Identify the blood parasite species.
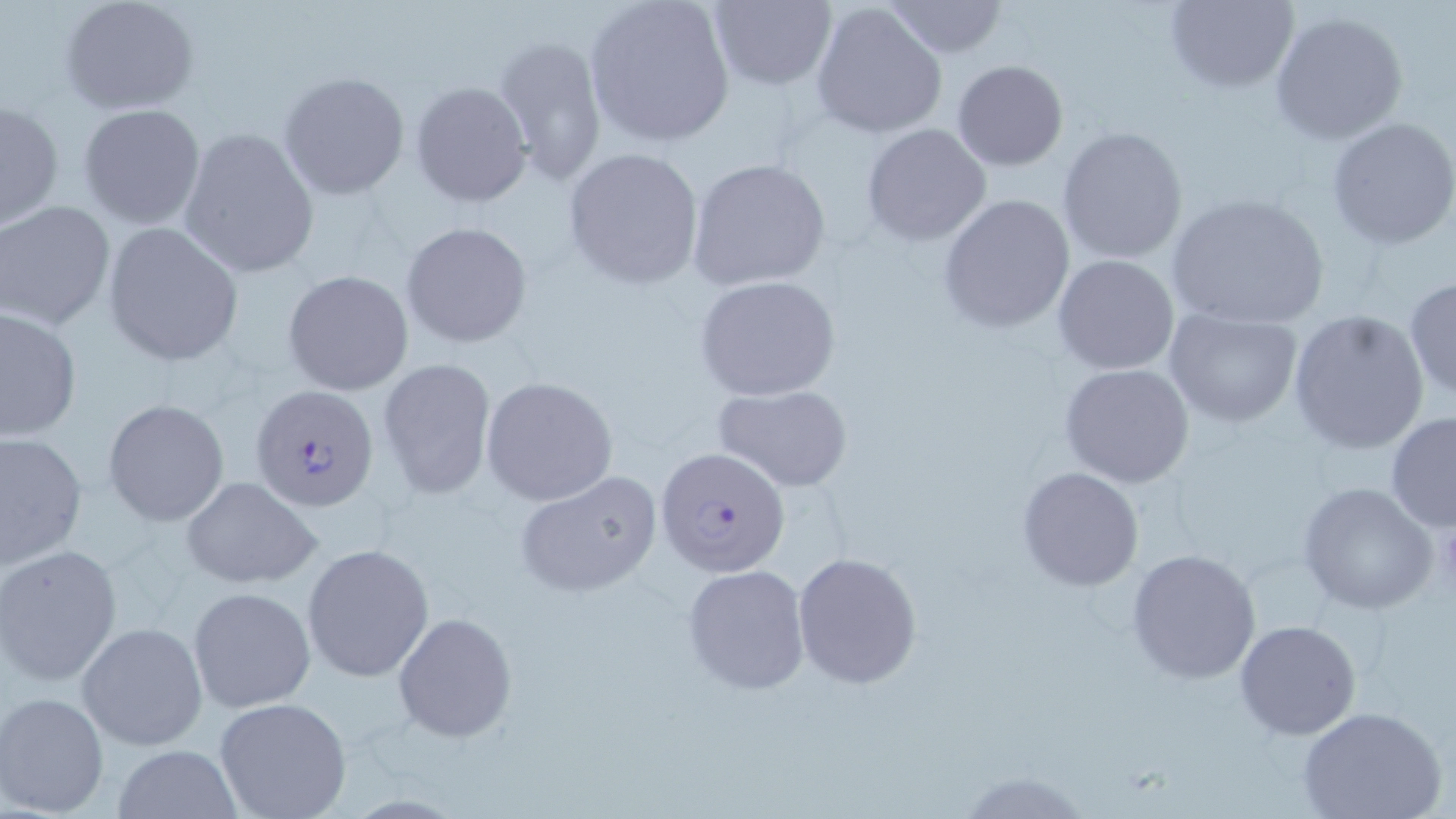

Plasmodium falciparum.

Approximate bounding boxes as named x1/y1/x2/y2 corners in pixels. Platelet locations: (x1=1438, y1=516, x2=1456, y2=598). Uninfected red blood cell locations: (x1=59, y1=0, x2=199, y2=114), (x1=586, y1=0, x2=737, y2=148), (x1=706, y1=0, x2=838, y2=91), (x1=809, y1=1, x2=949, y2=140), (x1=883, y1=1, x2=1008, y2=58), (x1=1162, y1=1, x2=1300, y2=93), (x1=1269, y1=10, x2=1408, y2=146), (x1=493, y1=34, x2=608, y2=187), (x1=953, y1=60, x2=1068, y2=170), (x1=278, y1=71, x2=410, y2=200), (x1=410, y1=80, x2=532, y2=208), (x1=1, y1=97, x2=64, y2=233), (x1=78, y1=103, x2=205, y2=229), (x1=1325, y1=116, x2=1456, y2=249), (x1=862, y1=123, x2=992, y2=246), (x1=1056, y1=126, x2=1188, y2=265), (x1=177, y1=128, x2=319, y2=279), (x1=563, y1=146, x2=705, y2=290), (x1=686, y1=158, x2=833, y2=293), (x1=938, y1=193, x2=1075, y2=334), (x1=1165, y1=193, x2=1331, y2=332), (x1=1, y1=201, x2=115, y2=330), (x1=102, y1=222, x2=243, y2=366), (x1=399, y1=222, x2=531, y2=349), (x1=1053, y1=256, x2=1179, y2=374), (x1=282, y1=270, x2=414, y2=395), (x1=695, y1=274, x2=841, y2=401), (x1=1404, y1=277, x2=1456, y2=403), (x1=0, y1=306, x2=81, y2=440), (x1=1162, y1=308, x2=1304, y2=428), (x1=1286, y1=308, x2=1431, y2=454), (x1=377, y1=356, x2=496, y2=500), (x1=1059, y1=364, x2=1195, y2=488), (x1=481, y1=376, x2=618, y2=506), (x1=714, y1=384, x2=851, y2=492), (x1=103, y1=399, x2=230, y2=527), (x1=1385, y1=411, x2=1456, y2=532), (x1=0, y1=430, x2=87, y2=573), (x1=1017, y1=467, x2=1143, y2=591), (x1=514, y1=469, x2=664, y2=598), (x1=179, y1=477, x2=321, y2=589), (x1=1298, y1=481, x2=1441, y2=615), (x1=302, y1=542, x2=435, y2=682), (x1=1, y1=544, x2=124, y2=687), (x1=1126, y1=548, x2=1262, y2=684), (x1=793, y1=552, x2=925, y2=690), (x1=682, y1=563, x2=810, y2=693), (x1=187, y1=586, x2=315, y2=712), (x1=393, y1=611, x2=517, y2=743), (x1=1234, y1=619, x2=1361, y2=739), (x1=77, y1=622, x2=207, y2=751), (x1=1, y1=692, x2=111, y2=817), (x1=213, y1=697, x2=352, y2=819), (x1=1300, y1=707, x2=1447, y2=819), (x1=111, y1=744, x2=242, y2=818). Plasmodium falciparum-infected red blood cell locations: (x1=250, y1=385, x2=381, y2=514), (x1=657, y1=445, x2=790, y2=578). May-Grünwald-Giemsa stain. Thin blood smear. Captured at 1000x magnification. Single field of view. Image is 1456×819 pixels. Optical microscopy.